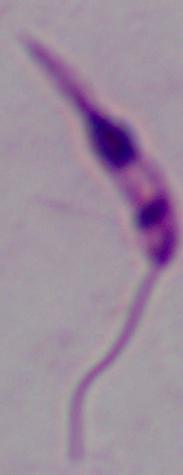

{
  "modality": "photomicrograph",
  "magnification": "1000x",
  "identification": "Leishmania"
}